Identify the blood parasite species.
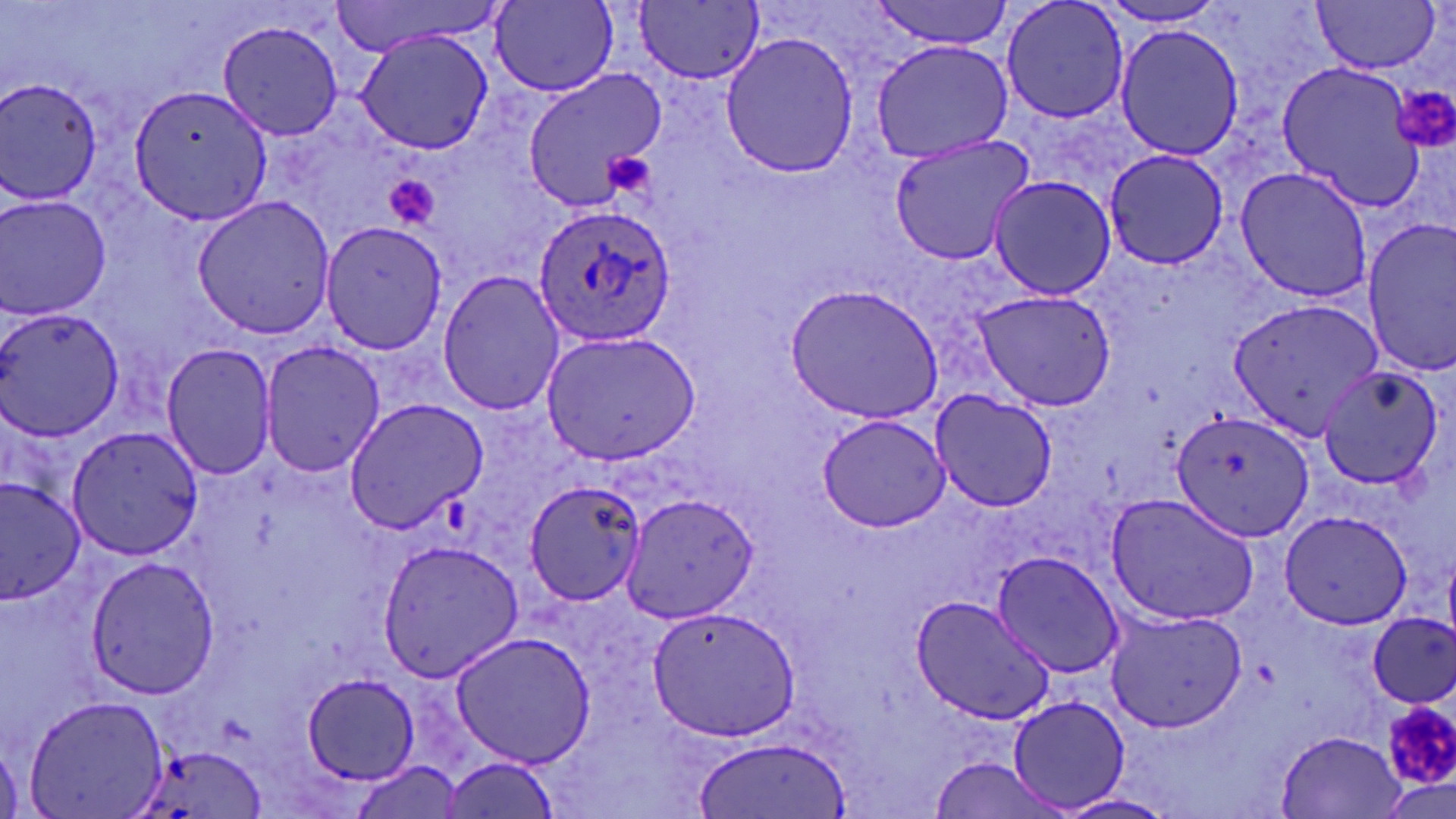

Plasmodium ovale.

modality = optical microscopy
field of view = single
stain = May-Grünwald-Giemsa
platelet locations = approximate bounding boxes as named x1/y1/x2/y2 corners in pixels: (x1=1394, y1=85, x2=1456, y2=149), (x1=604, y1=151, x2=656, y2=204), (x1=382, y1=171, x2=443, y2=234), (x1=1379, y1=704, x2=1456, y2=798)
magnification = 1000x
Plasmodium ovale-infected red blood cell locations = approximate bounding boxes as named x1/y1/x2/y2 corners in pixels: (x1=531, y1=202, x2=679, y2=347)
image size = 1456×819 pixels
uninfected red blood cell locations = approximate bounding boxes as named x1/y1/x2/y2 corners in pixels: (x1=326, y1=0, x2=511, y2=55), (x1=870, y1=0, x2=1015, y2=49), (x1=999, y1=0, x2=1132, y2=125), (x1=1311, y1=0, x2=1440, y2=74), (x1=491, y1=1, x2=618, y2=94), (x1=635, y1=2, x2=763, y2=85), (x1=1091, y1=3, x2=1236, y2=28), (x1=215, y1=17, x2=342, y2=140), (x1=1112, y1=21, x2=1245, y2=162), (x1=354, y1=28, x2=493, y2=157), (x1=719, y1=31, x2=858, y2=180), (x1=869, y1=40, x2=1013, y2=164), (x1=1272, y1=60, x2=1427, y2=209), (x1=523, y1=69, x2=668, y2=208), (x1=2, y1=77, x2=109, y2=208), (x1=130, y1=85, x2=272, y2=224), (x1=887, y1=134, x2=1035, y2=265), (x1=1103, y1=151, x2=1233, y2=271), (x1=1234, y1=166, x2=1373, y2=303), (x1=987, y1=174, x2=1116, y2=302), (x1=1, y1=192, x2=113, y2=320), (x1=191, y1=196, x2=338, y2=340), (x1=322, y1=220, x2=447, y2=355), (x1=1361, y1=221, x2=1455, y2=377), (x1=436, y1=270, x2=564, y2=417), (x1=784, y1=284, x2=943, y2=425), (x1=972, y1=289, x2=1115, y2=410), (x1=1230, y1=298, x2=1385, y2=439), (x1=1, y1=306, x2=123, y2=441), (x1=537, y1=329, x2=701, y2=466), (x1=258, y1=339, x2=385, y2=479), (x1=160, y1=342, x2=277, y2=479), (x1=1315, y1=367, x2=1443, y2=491), (x1=929, y1=390, x2=1057, y2=513), (x1=342, y1=399, x2=488, y2=533), (x1=1170, y1=410, x2=1314, y2=542), (x1=815, y1=411, x2=952, y2=533), (x1=67, y1=424, x2=202, y2=559), (x1=0, y1=475, x2=85, y2=607), (x1=523, y1=480, x2=650, y2=608), (x1=1104, y1=491, x2=1260, y2=627), (x1=619, y1=495, x2=759, y2=627), (x1=1278, y1=508, x2=1416, y2=632), (x1=375, y1=537, x2=522, y2=682), (x1=993, y1=552, x2=1126, y2=676), (x1=83, y1=555, x2=223, y2=699), (x1=909, y1=595, x2=1054, y2=723), (x1=647, y1=603, x2=798, y2=743), (x1=1105, y1=607, x2=1247, y2=732), (x1=1368, y1=613, x2=1456, y2=709), (x1=449, y1=630, x2=596, y2=767), (x1=302, y1=672, x2=421, y2=784), (x1=23, y1=693, x2=167, y2=818), (x1=1009, y1=696, x2=1130, y2=811), (x1=1279, y1=730, x2=1407, y2=817), (x1=695, y1=737, x2=851, y2=817), (x1=127, y1=743, x2=262, y2=819), (x1=441, y1=753, x2=563, y2=819), (x1=927, y1=757, x2=1065, y2=819), (x1=352, y1=760, x2=466, y2=816), (x1=1054, y1=793, x2=1179, y2=819)
preparation = thin blood film